State which parasite is depicted.
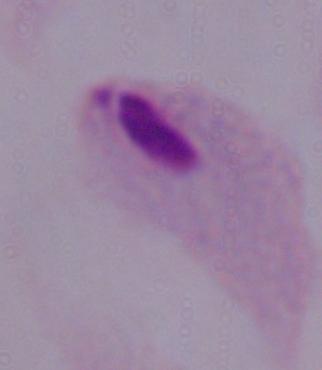
This is a trichomonad.

{
  "modality": "photomicrograph",
  "magnification": "1000x"
}